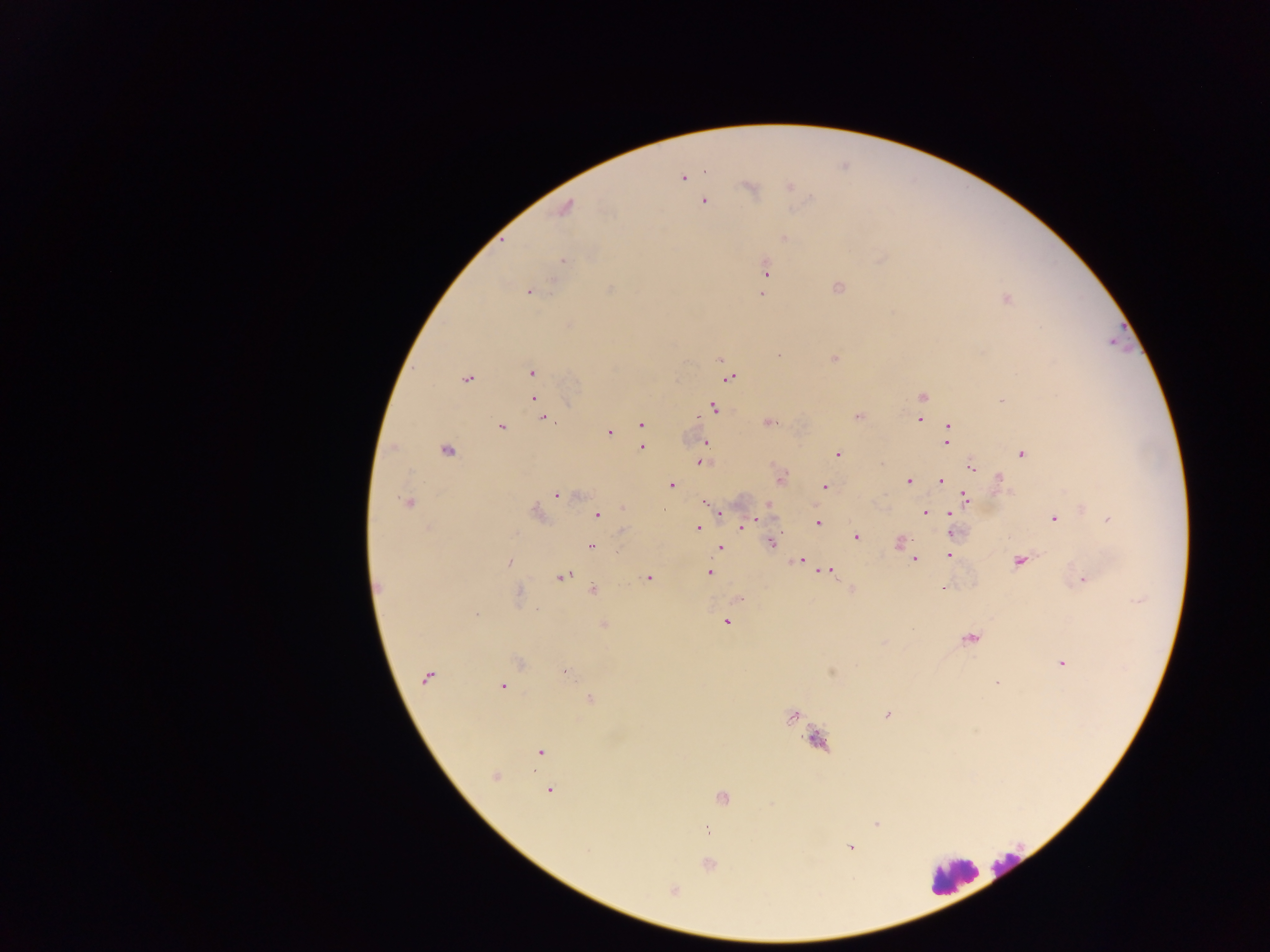
preparation = thick blood smear
image size = 1270×952 pixels
field of view = single
capture = mobile-phone photograph through a microscope
country = Ghana
malaria parasite locations = approximate centers as x y in pixels: 683 178; 748 187; 703 201; 564 209; 562 260; 765 271; 835 288; 609 289; 529 291; 761 295; 1005 298; 833 358; 720 360; 531 372; 728 377; 466 379; 923 396; 533 399; 1002 404; 713 406; 542 417; 857 418; 918 418; 768 421; 641 423; 502 425; 946 425; 609 433; 706 442; 947 444; 393 447; 448 449; 642 449; 1021 454; 838 455; 883 462; 701 463; 973 468; 999 477; 941 481; 909 482; 671 485; 825 486; 556 495; 965 496; 408 502; 766 504; 1080 508; 537 511; 719 512; 925 513; 949 514; 596 515; 1054 518; 1107 518; 756 519; 819 522; 745 523; 740 527; 699 528; 623 531; 854 535; 771 541; 899 542; 592 546; 718 547; 911 555; 948 556; 795 559; 801 560; 914 560; 1018 561; 511 562; 822 569; 828 570; 710 574; 563 577; 649 577; 1083 579; 944 589; 592 591; 520 595; 479 614; 726 623; 603 625; 970 639; 1060 662; 831 671; 572 676; 426 679; 995 683; 502 687; 590 699; 886 714; 792 717; 974 732; 815 740; 541 752; 497 776; 549 789; 722 797; 771 805; 878 822; 707 830; 851 848; 711 865; 673 891
leukocyte locations = approximate centers as x y in pixels: 951 867